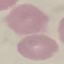
result = no malaria parasites detected
capture = smartphone through the microscope eyepiece
preparation = thin blood film
image type = automatically extracted cell patch, resized to 64 × 64 pixels
stain = Giemsa